Name the parasite shown.
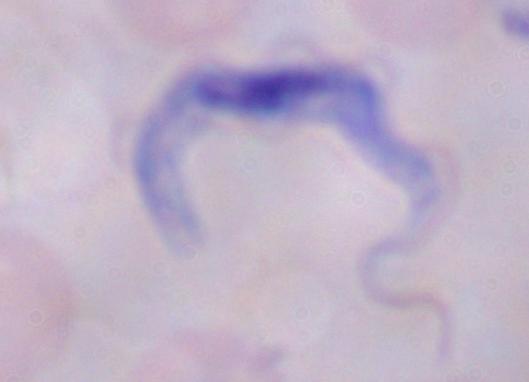

A trypanosome.

magnification = 1000x
modality = photomicrograph